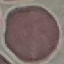
Result: negative for malaria parasites. Giemsa stain. Photographed with a smartphone camera at the microscope eyepiece. Cell patch, automatically extracted from a larger field of view and resized to 64 × 64 pixels. Thin blood smear.